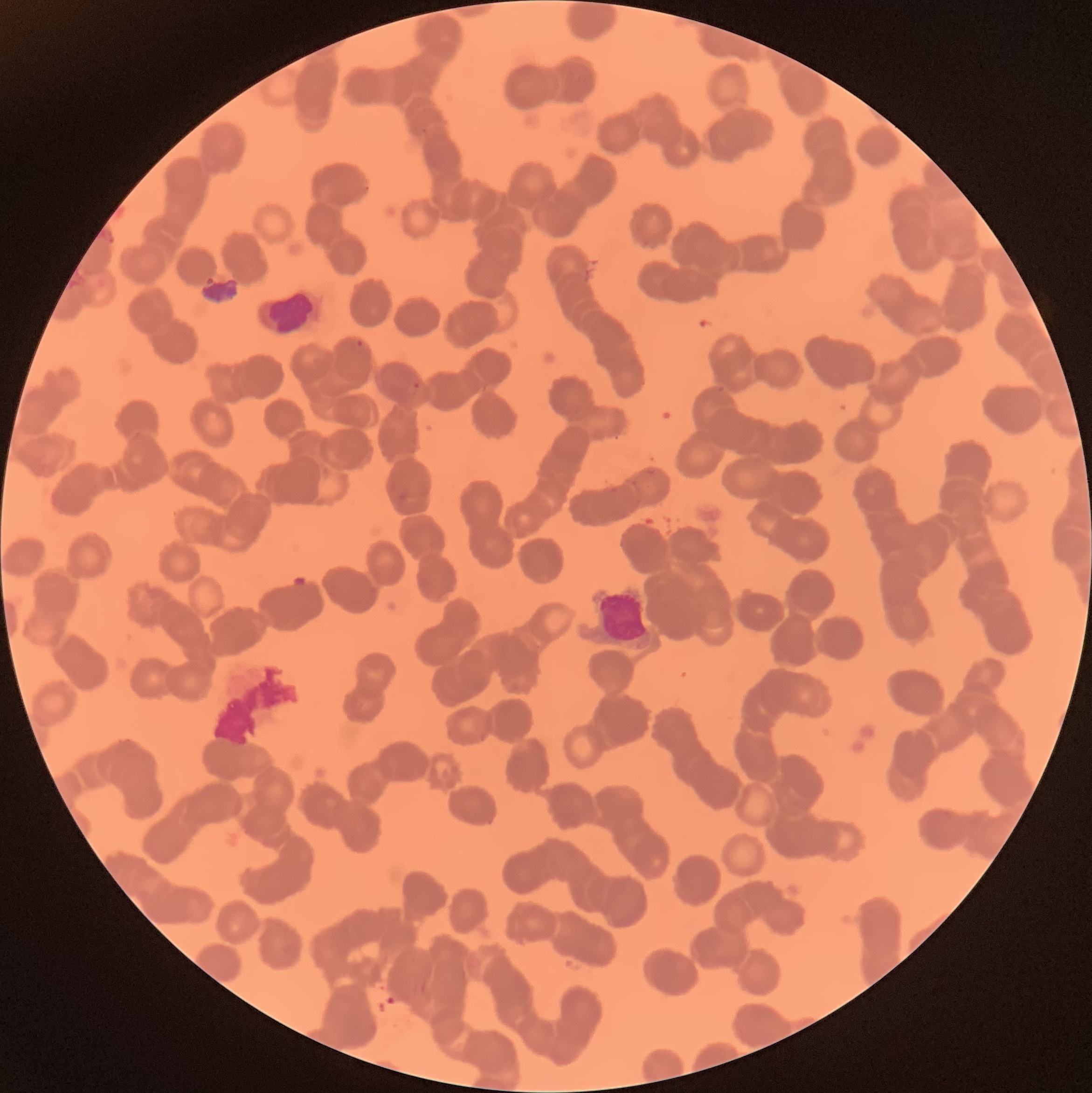

Summary:
  - Coordinate format: approximate bounding boxes as named x1/y1/x2/y2 corners in pixels
  - Plasmodium parasite locations: (x1=356, y1=339, x2=364, y2=349), (x1=412, y1=382, x2=421, y2=389)
  - White blood cell locations: (x1=257, y1=292, x2=321, y2=340)
  - Red blood cell morphology: rouleaux formation
  - Modality: optical microscopy
  - Image size: 1092×1093 pixels
  - Preparation: thin blood smear